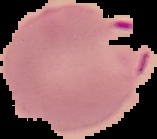

From a thin blood smear. Image is 157×139 pixels. Cell region segmented out of the field of view; the surrounding area is masked to black. Result: malaria parasites detected.